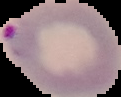 Segmented cell region on a black background. From a thin blood smear. Malaria status: parasitized. Image is 121×97 pixels.